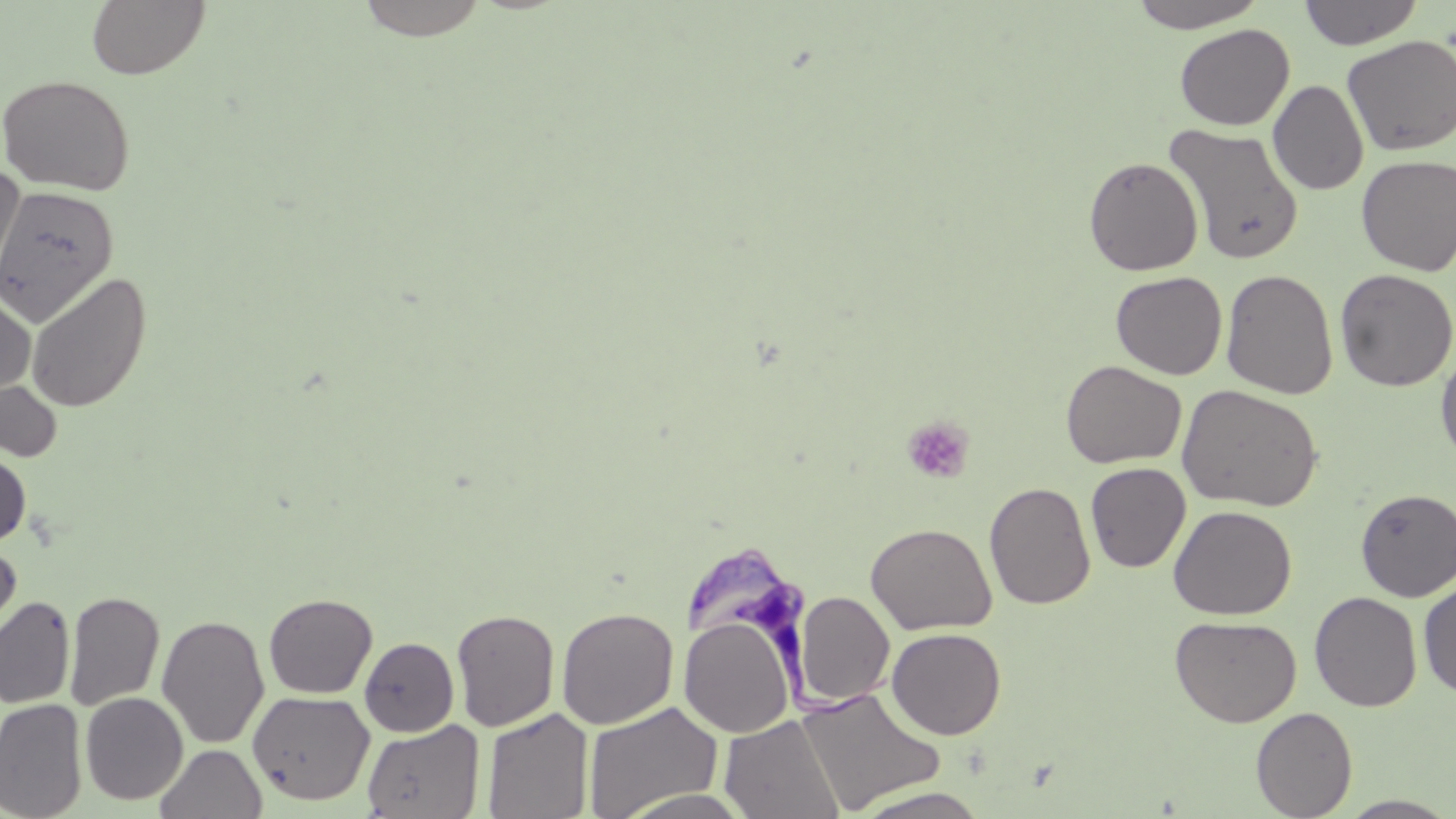
Trypanosoma brucei locations = approximate bounding boxes as [x1, y1, x2, y2] in pixels: [689, 542, 900, 723]
slide-level diagnosis = Trypanosoma brucei
field of view = one of a larger specimen
magnification = 1000x
preparation = thin blood smear
image size = 1456×819 pixels
uninfected red blood cell locations = approximate bounding boxes as [x1, y1, x2, y2] in pixels: [86, 0, 210, 79], [355, 0, 491, 41], [1129, 0, 1268, 32], [1298, 0, 1423, 49], [1174, 24, 1294, 131], [1341, 34, 1456, 156], [0, 74, 136, 196], [1268, 80, 1369, 195], [1164, 123, 1305, 266], [1356, 154, 1456, 276], [1083, 156, 1203, 276], [0, 167, 25, 290], [0, 185, 119, 326], [1220, 267, 1338, 399], [1334, 269, 1456, 392], [25, 271, 152, 414], [1110, 271, 1227, 380], [0, 289, 35, 397], [1436, 347, 1456, 465], [1061, 360, 1186, 469], [0, 380, 62, 462], [1177, 383, 1323, 511], [0, 448, 31, 548], [1085, 462, 1191, 573], [984, 481, 1096, 610], [1355, 488, 1456, 601], [1168, 504, 1297, 620], [866, 522, 995, 635], [0, 542, 22, 645], [1418, 578, 1456, 699], [64, 590, 165, 711], [794, 591, 895, 706], [1309, 591, 1422, 712], [263, 593, 377, 698], [0, 596, 76, 709], [556, 606, 679, 729], [451, 608, 560, 732], [156, 614, 270, 748], [1170, 614, 1303, 727], [679, 615, 796, 738], [886, 627, 1007, 739], [359, 637, 459, 737], [795, 686, 945, 814], [247, 690, 375, 805], [80, 692, 188, 805], [0, 698, 87, 819], [583, 701, 724, 818], [482, 707, 594, 819], [1250, 707, 1358, 818], [719, 714, 844, 819], [362, 718, 485, 819], [157, 744, 266, 819], [848, 787, 993, 818], [611, 789, 754, 819], [1335, 795, 1456, 818]
stain = May-Grünwald-Giemsa
platelet locations = approximate bounding boxes as [x1, y1, x2, y2] in pixels: [901, 416, 975, 484]
modality = optical microscopy